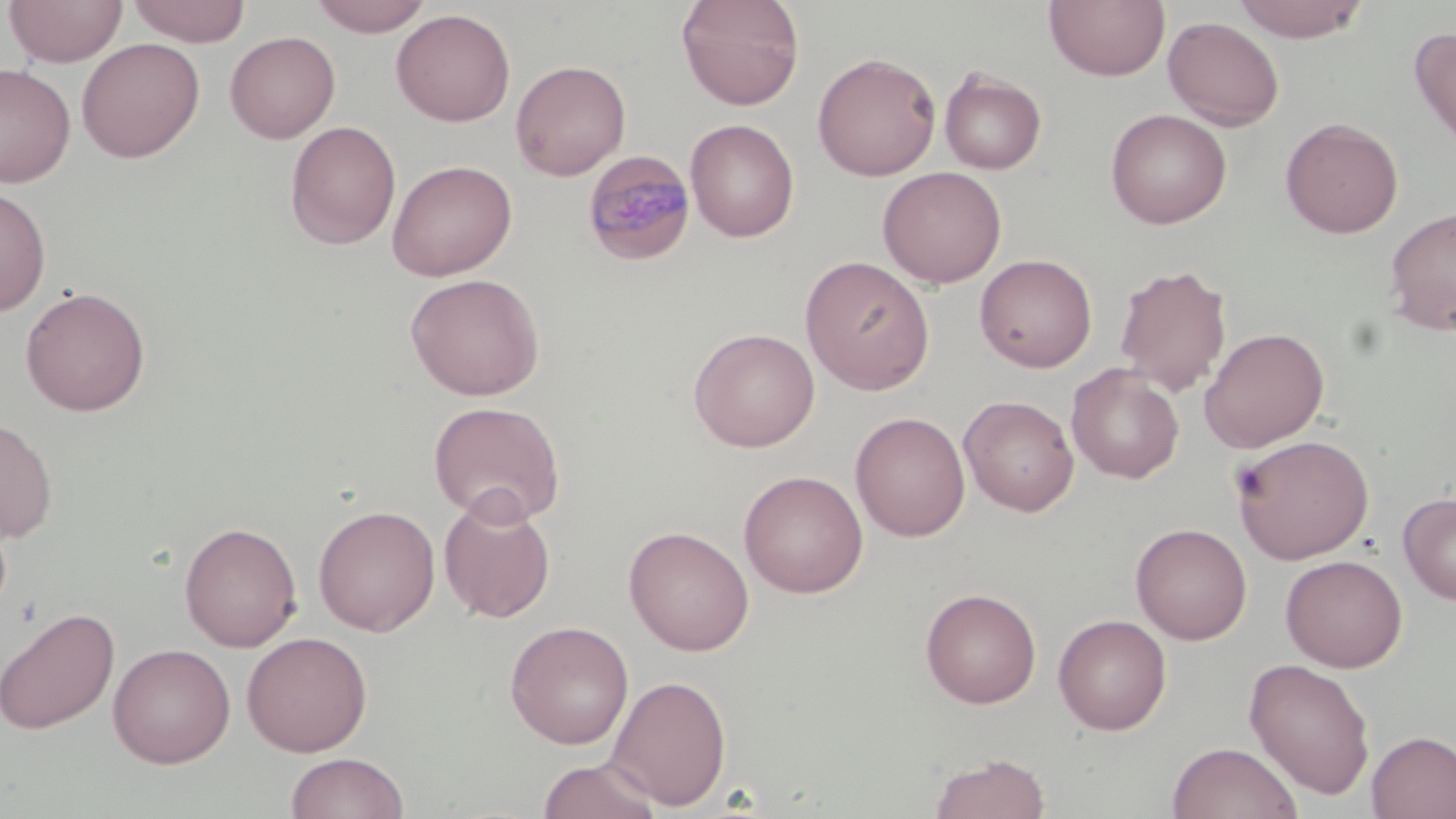
Approximate bounding boxes as named x1/y1/x2/y2 corners in pixels. Plasmodium malariae-infected red blood cell locations: (x1=582, y1=149, x2=697, y2=266). Uninfected red blood cell locations: (x1=3, y1=0, x2=129, y2=67), (x1=126, y1=0, x2=251, y2=46), (x1=308, y1=0, x2=434, y2=37), (x1=676, y1=0, x2=805, y2=110), (x1=1044, y1=0, x2=1170, y2=81), (x1=1231, y1=1, x2=1369, y2=43), (x1=391, y1=9, x2=515, y2=126), (x1=1163, y1=16, x2=1285, y2=131), (x1=1408, y1=26, x2=1456, y2=157), (x1=224, y1=31, x2=341, y2=143), (x1=76, y1=38, x2=205, y2=163), (x1=812, y1=52, x2=941, y2=181), (x1=510, y1=59, x2=631, y2=181), (x1=0, y1=62, x2=76, y2=187), (x1=939, y1=66, x2=1047, y2=175), (x1=1105, y1=108, x2=1232, y2=229), (x1=1280, y1=117, x2=1403, y2=238), (x1=685, y1=118, x2=799, y2=242), (x1=285, y1=121, x2=401, y2=251), (x1=386, y1=159, x2=517, y2=281), (x1=877, y1=166, x2=1007, y2=287), (x1=0, y1=184, x2=52, y2=316), (x1=1384, y1=206, x2=1456, y2=336), (x1=974, y1=254, x2=1097, y2=373), (x1=800, y1=255, x2=935, y2=394), (x1=1114, y1=263, x2=1232, y2=396), (x1=405, y1=272, x2=545, y2=401), (x1=20, y1=286, x2=151, y2=416), (x1=688, y1=327, x2=820, y2=452), (x1=1199, y1=327, x2=1330, y2=453), (x1=1066, y1=364, x2=1185, y2=483), (x1=959, y1=395, x2=1079, y2=516), (x1=428, y1=400, x2=566, y2=527), (x1=850, y1=411, x2=970, y2=542), (x1=0, y1=416, x2=58, y2=543), (x1=1232, y1=434, x2=1374, y2=563), (x1=738, y1=470, x2=869, y2=598), (x1=1398, y1=491, x2=1456, y2=605), (x1=438, y1=493, x2=556, y2=623), (x1=313, y1=504, x2=440, y2=636), (x1=179, y1=521, x2=302, y2=652), (x1=1130, y1=522, x2=1253, y2=644), (x1=623, y1=525, x2=755, y2=656), (x1=1280, y1=555, x2=1407, y2=672), (x1=920, y1=587, x2=1041, y2=708), (x1=0, y1=606, x2=120, y2=735), (x1=1053, y1=614, x2=1172, y2=735), (x1=504, y1=620, x2=634, y2=749), (x1=241, y1=631, x2=372, y2=756), (x1=107, y1=642, x2=236, y2=767), (x1=1243, y1=657, x2=1376, y2=800), (x1=605, y1=674, x2=732, y2=811), (x1=1366, y1=730, x2=1456, y2=819), (x1=1166, y1=741, x2=1302, y2=819), (x1=285, y1=752, x2=410, y2=818), (x1=927, y1=752, x2=1052, y2=819), (x1=536, y1=757, x2=663, y2=819). Slide-level diagnosis: Plasmodium malariae. Thin blood smear. Single field of view. Light microscopy. Captured at 1000x magnification. May-Grünwald-Giemsa-stained preparation. Image is 1456×819 pixels.